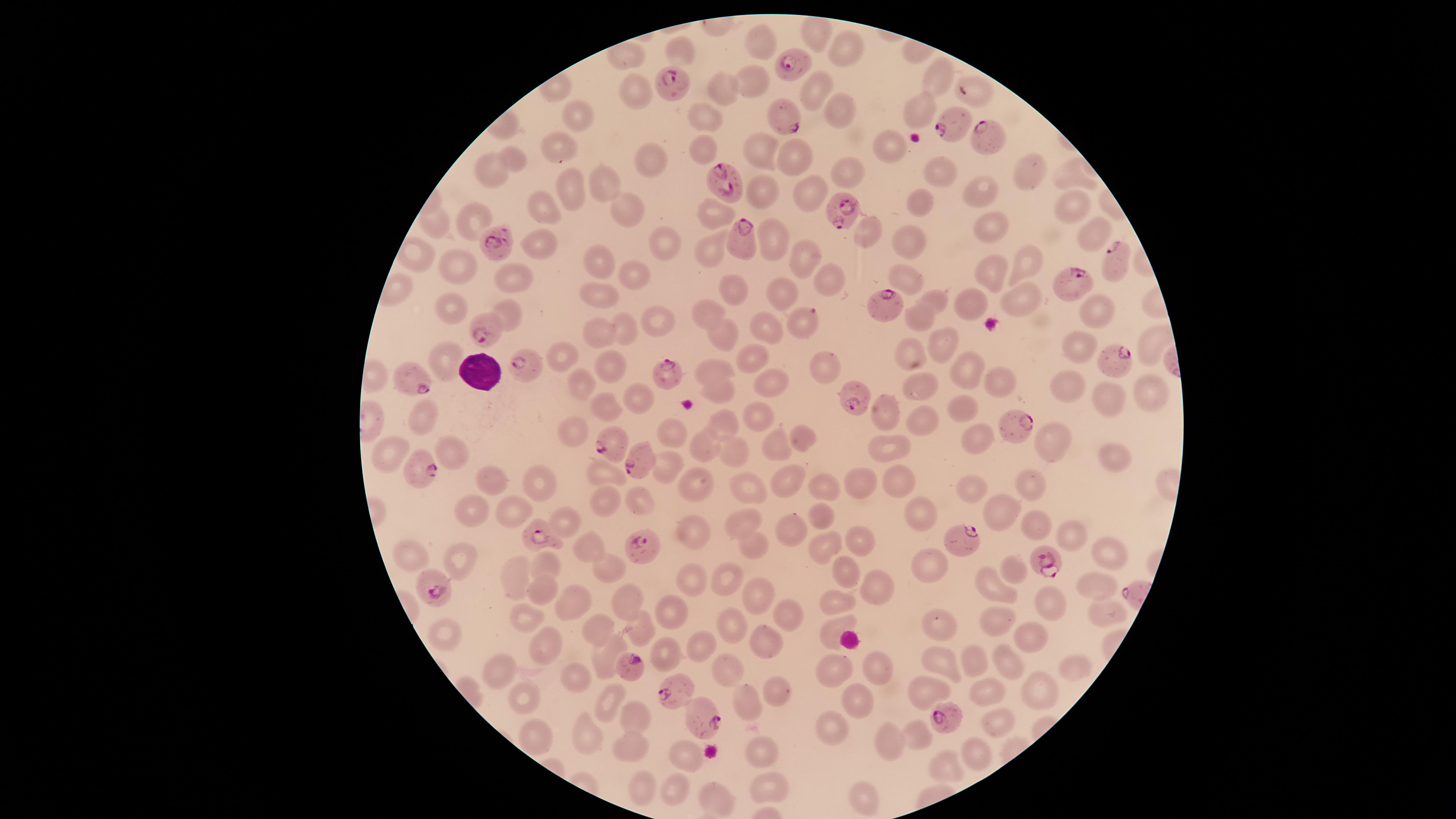 Approximate marker points as {x, y} in pixels. Uninfected red blood cells: {817, 27}, {755, 39}, {847, 48}, {938, 76}, {751, 81}, {810, 87}, {717, 92}, {634, 94}, {918, 108}, {836, 111}, {572, 115}, {702, 116}, {885, 140}, {696, 144}, {560, 147}, {758, 148}, {789, 155}, {514, 157}, {654, 157}, {492, 170}, {940, 172}, {1032, 172}, {843, 173}, {1068, 174}, {602, 183}, {565, 187}, {982, 190}, {807, 193}, {757, 194}, {922, 204}, {541, 206}, {625, 207}, {1074, 208}, {710, 211}, {474, 218}, {434, 224}, {986, 224}, {863, 228}, {1092, 233}, {768, 238}, {661, 241}, {542, 242}, {908, 246}, {715, 251}, {806, 257}, {598, 262}, {1028, 262}, {454, 266}, {989, 272}, {631, 273}, {905, 276}, {822, 278}, {516, 281}, {733, 291}, {603, 293}, {777, 295}, {1017, 295}, {936, 301}, {971, 301}, {1099, 307}, {452, 309}, {508, 309}, {706, 314}, {918, 316}, {655, 319}, {622, 326}, {766, 326}, {600, 329}, {717, 335}, {1148, 341}, {940, 342}, {1077, 347}, {909, 350}, {563, 356}, {747, 356}, {448, 361}, {820, 362}, {609, 364}, {965, 367}, {710, 369}, {579, 380}, {1005, 381}, {771, 382}, {1062, 385}, {928, 389}, {717, 390}, {629, 394}, {1108, 394}, {1150, 396}, {605, 408}, {965, 409}, {888, 411}, {758, 414}, {424, 416}, {919, 416}, {723, 419}, {569, 429}, {671, 430}, {802, 434}, {1045, 437}, {779, 443}, {976, 444}, {704, 447}, {896, 451}, {393, 452}, {455, 452}, {734, 452}, {1109, 452}, {665, 470}, {607, 473}, {532, 477}, {896, 477}, {782, 478}, {745, 479}, {858, 480}, {497, 482}, {822, 484}, {1033, 485}, {694, 486}, {974, 491}, {606, 498}, {643, 501}, {998, 510}, {472, 511}, {922, 511}, {514, 515}, {824, 516}, {563, 521}, {738, 521}, {688, 525}, {1032, 526}, {795, 529}, {1070, 533}, {747, 539}, {860, 541}, {823, 545}, {1107, 546}, {585, 547}, {405, 554}, {463, 556}, {546, 562}, {1014, 563}, {928, 567}, {608, 569}, {513, 573}, {726, 579}, {847, 579}, {691, 581}, {878, 584}, {1104, 584}, {539, 587}, {994, 587}, {756, 595}, {630, 600}, {1055, 600}, {575, 604}, {832, 606}, {670, 609}, {1111, 611}, {789, 619}, {528, 621}, {1005, 622}, {941, 625}, {1035, 626}, {734, 627}, {593, 628}, {641, 629}, {831, 630}, {443, 632}, {759, 637}, {537, 646}, {698, 647}, {661, 654}, {606, 657}, {974, 658}, {943, 661}, {1004, 663}, {1069, 663}, {727, 666}, {883, 670}, {833, 671}, {498, 672}, {577, 678}, {1042, 688}, {770, 689}, {922, 689}, {989, 691}, {525, 700}, {608, 700}, {860, 701}, {748, 702}, {630, 715}, {997, 724}, {832, 725}, {591, 736}, {918, 736}, {538, 738}, {891, 743}, {631, 745}, {757, 749}, {974, 752}, {684, 757}, {941, 765}, {771, 784}, {643, 787}, {671, 788}, {863, 799}, {716, 802}. White blood cells: {476, 371}. Parasitized red blood cells: {790, 59}, {674, 81}, {977, 92}, {786, 117}, {953, 123}, {982, 136}, {725, 180}, {840, 206}, {738, 236}, {497, 242}, {1110, 262}, {1067, 283}, {881, 307}, {803, 321}, {484, 327}, {1108, 359}, {523, 365}, {668, 372}, {411, 379}, {853, 391}, {1011, 422}, {614, 443}, {638, 461}, {417, 468}, {538, 536}, {961, 543}, {641, 546}, {1042, 560}, {438, 588}, {631, 665}, {679, 693}, {948, 718}, {710, 720}. One field of view of the specimen. Presence: malaria parasites seen. Image is 1456×819 pixels. Thin smear of blood. Circular visible region. Giemsa-stained preparation. Species: Plasmodium falciparum. Photographed with a smartphone camera through the microscope eyepiece.